Name the blood parasite species.
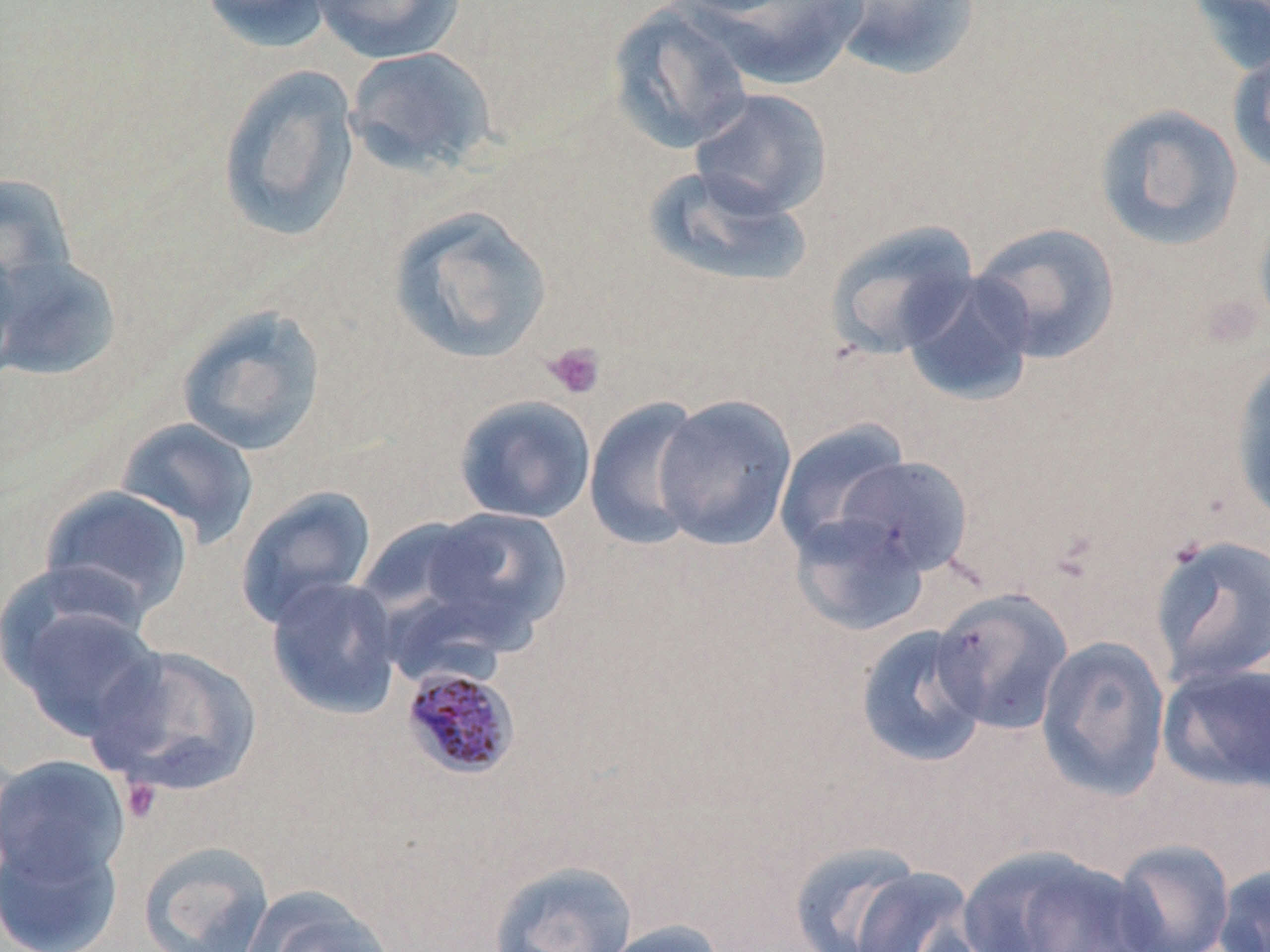
Plasmodium malariae.

{
  "field_of_view": "one of a larger specimen",
  "stain": "May-Grünwald-Giemsa",
  "modality": "light microscopy",
  "uninfected_red_blood_cell_locations": "approximate bounding boxes as (x1, y1, x2, y2) in pixels: (197, 0, 336, 53), (309, 0, 466, 64), (681, 0, 869, 89), (826, 0, 982, 80), (1186, 0, 1270, 77), (606, 3, 756, 155), (1227, 43, 1270, 179), (343, 46, 497, 176), (217, 64, 362, 245), (689, 88, 833, 219), (1093, 103, 1244, 252), (642, 165, 813, 290), (0, 172, 78, 300), (387, 204, 555, 365), (1253, 208, 1270, 337), (823, 219, 980, 361), (970, 221, 1122, 365), (0, 235, 24, 380), (0, 251, 120, 382), (899, 270, 1037, 406), (174, 303, 328, 457), (1230, 351, 1270, 528), (653, 393, 797, 551), (453, 394, 596, 524), (584, 396, 709, 551), (114, 416, 260, 549), (773, 419, 912, 560), (833, 455, 973, 576), (38, 485, 196, 621), (234, 485, 377, 630), (405, 505, 573, 648), (789, 513, 931, 637), (1148, 533, 1270, 688), (265, 576, 403, 719), (929, 586, 1074, 735), (3, 591, 165, 742), (854, 624, 990, 767), (1035, 634, 1172, 801), (84, 643, 263, 797), (1158, 661, 1270, 794), (0, 753, 131, 903), (0, 826, 125, 952), (786, 839, 931, 952), (138, 840, 275, 952), (1110, 840, 1236, 952), (955, 845, 1159, 952), (487, 860, 639, 952), (1212, 863, 1270, 952), (848, 866, 985, 952), (240, 887, 401, 952), (596, 920, 729, 952)",
  "image_size": "1270×952 pixels",
  "preparation": "thin blood smear",
  "magnification": "1000x",
  "platelet_locations": "approximate bounding boxes as (x1, y1, x2, y2) in pixels: (542, 341, 605, 400), (120, 776, 164, 824)",
  "plasmodium_malariae_infected_red_blood_cell_locations": "approximate bounding boxes as (x1, y1, x2, y2) in pixels: (400, 665, 522, 781)"
}